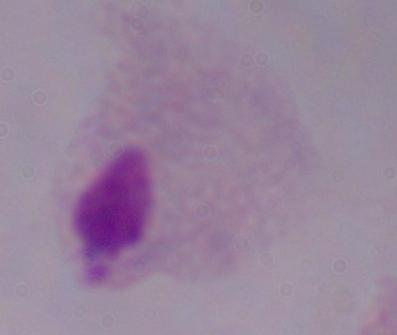

Photomicrograph. 1000x magnification. A trichomonad is shown.